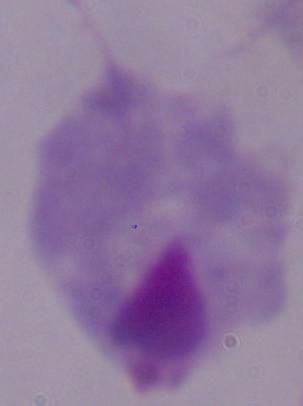
identification = trichomonad
modality = photomicrograph
magnification = 1000x